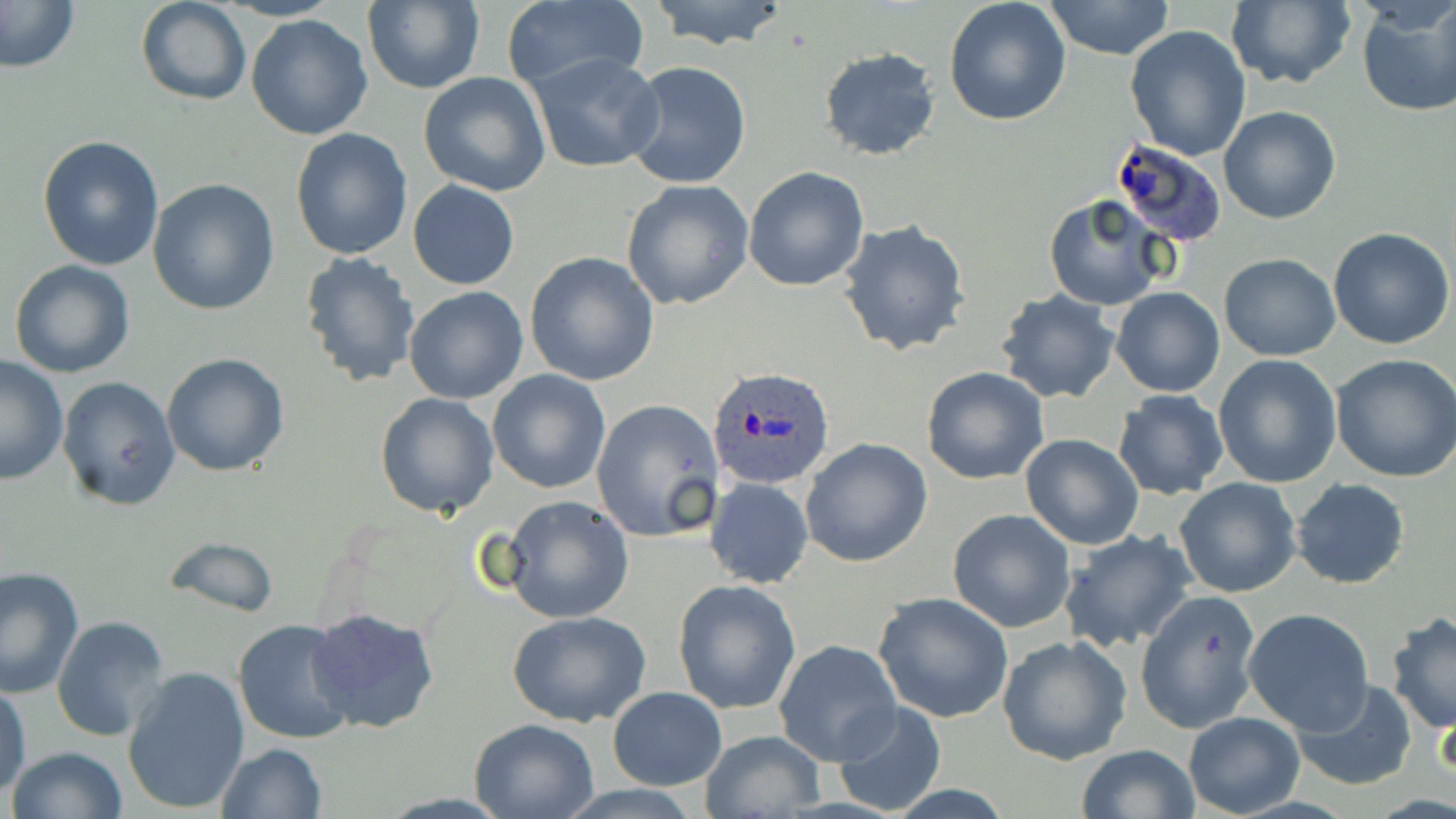
slide-level diagnosis = Plasmodium ovale
magnification = 1000x
image size = 1456×819 pixels
Plasmodium ovale-infected red blood cell locations = approximate bounding boxes as [x1, y1, x2, y2] in pixels: [1110, 141, 1228, 248], [706, 364, 838, 491]
field of view = one of a larger specimen
modality = light microscopy
stain = May-Grünwald-Giemsa
preparation = thin blood smear
uninfected red blood cell locations = approximate bounding boxes as [x1, y1, x2, y2] in pixels: [0, 0, 80, 75], [135, 0, 251, 106], [644, 0, 793, 51], [944, 0, 1072, 125], [1043, 0, 1176, 60], [1224, 0, 1356, 90], [360, 1, 485, 93], [500, 2, 649, 96], [1355, 2, 1456, 118], [246, 13, 375, 140], [1125, 24, 1253, 160], [818, 47, 942, 161], [528, 53, 666, 173], [622, 61, 751, 190], [418, 72, 551, 195], [1218, 105, 1342, 224], [290, 128, 413, 262], [36, 136, 164, 270], [743, 166, 869, 292], [148, 179, 280, 316], [408, 180, 520, 289], [620, 180, 755, 310], [1043, 194, 1170, 311], [838, 219, 970, 357], [1329, 228, 1455, 349], [298, 251, 421, 388], [524, 252, 660, 389], [1218, 253, 1341, 362], [8, 259, 136, 379], [404, 286, 529, 404], [1113, 286, 1224, 397], [996, 290, 1121, 405], [161, 353, 290, 477], [1329, 353, 1456, 483], [1213, 354, 1343, 488], [1, 356, 69, 486], [921, 366, 1050, 485], [488, 369, 612, 494], [57, 376, 181, 511], [1112, 389, 1228, 500], [374, 392, 500, 517], [591, 398, 725, 544], [1019, 434, 1145, 550], [801, 438, 933, 568], [705, 477, 814, 590], [1174, 477, 1302, 597], [1291, 478, 1409, 589], [500, 494, 634, 622], [946, 509, 1076, 631], [1059, 527, 1197, 651], [166, 535, 281, 618], [0, 566, 84, 697], [673, 580, 801, 717], [1135, 590, 1263, 733], [873, 592, 1015, 723], [306, 607, 441, 733], [1242, 608, 1375, 735], [507, 609, 653, 728], [1385, 612, 1456, 735], [51, 615, 171, 742], [233, 618, 360, 745], [997, 633, 1133, 765], [775, 639, 901, 765], [121, 665, 251, 816], [1290, 678, 1419, 791], [0, 685, 31, 802], [609, 686, 727, 789], [831, 699, 948, 816], [1183, 710, 1305, 816], [468, 718, 600, 819], [701, 730, 825, 816], [215, 742, 326, 819], [1076, 744, 1201, 819], [8, 746, 128, 819]